State the blood parasite species.
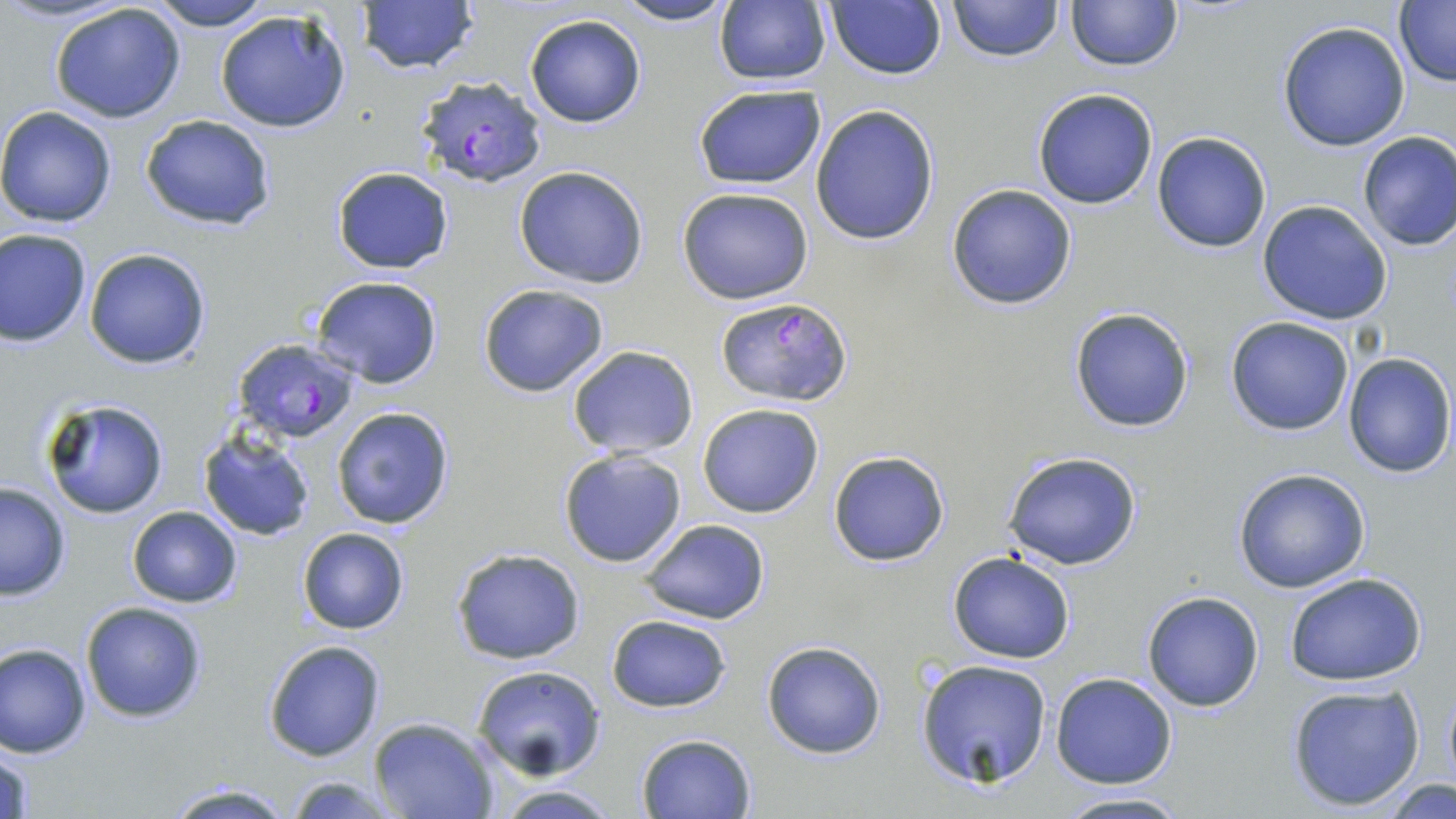
Plasmodium falciparum.

{
  "modality": "light microscopy",
  "stain": "May-Grünwald-Giemsa",
  "image_size": "1456×819 pixels",
  "magnification": "1000x",
  "uninfected_red_blood_cell_locations": "approximate bounding boxes as [x1, y1, x2, y2] in pixels: [144, 0, 276, 30], [612, 0, 739, 27], [948, 0, 1061, 62], [1065, 0, 1182, 71], [354, 1, 480, 76], [712, 2, 831, 86], [823, 2, 947, 81], [1394, 2, 1456, 84], [47, 3, 189, 122], [215, 8, 355, 134], [525, 15, 646, 127], [1277, 21, 1412, 152], [693, 85, 826, 190], [1031, 87, 1160, 209], [809, 103, 940, 247], [0, 105, 121, 227], [140, 114, 276, 233], [1151, 131, 1273, 254], [1356, 131, 1456, 252], [513, 166, 650, 289], [331, 167, 454, 274], [946, 183, 1078, 311], [677, 186, 815, 305], [1257, 200, 1393, 325], [0, 228, 92, 346], [83, 246, 213, 368], [310, 276, 442, 388], [478, 282, 610, 398], [1068, 305, 1196, 433], [1226, 315, 1354, 436], [566, 346, 698, 459], [1340, 351, 1454, 477], [39, 395, 171, 519], [696, 402, 826, 519], [330, 406, 456, 530], [197, 427, 318, 541], [556, 449, 689, 570], [827, 451, 951, 567], [1004, 453, 1143, 570], [1231, 468, 1373, 593], [0, 482, 71, 599], [127, 504, 243, 608], [641, 519, 770, 625], [297, 527, 408, 635], [450, 548, 587, 663], [947, 551, 1075, 663], [1282, 571, 1431, 686], [1141, 591, 1264, 712], [79, 600, 207, 722], [606, 615, 731, 712], [261, 639, 385, 761], [761, 640, 888, 760], [1, 642, 93, 758], [914, 658, 1054, 788], [472, 664, 607, 781], [1051, 673, 1178, 788], [1286, 683, 1427, 812], [367, 716, 500, 819], [635, 732, 757, 818], [1, 743, 34, 819], [283, 775, 409, 816], [1376, 776, 1454, 817], [161, 781, 296, 818], [489, 783, 624, 817], [1050, 791, 1195, 819]",
  "field_of_view": "one of a larger specimen",
  "preparation": "thin blood smear",
  "plasmodium_falciparum_infected_red_blood_cell_locations": "approximate bounding boxes as [x1, y1, x2, y2] in pixels: [416, 76, 547, 187], [714, 295, 854, 408], [232, 339, 360, 446]"
}